Outline each Plasmodium falciparum-infected red blood cell.
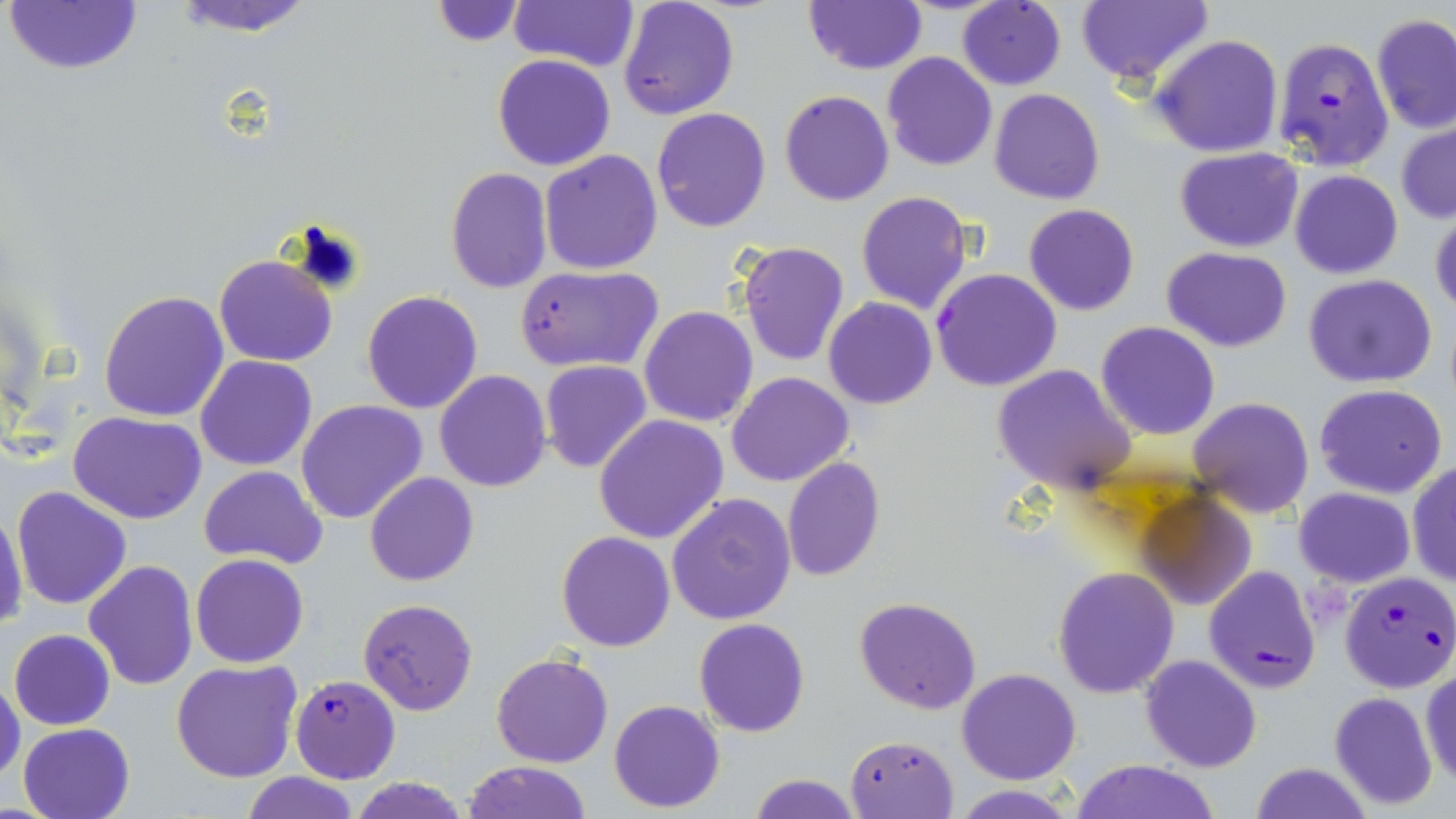

Approximate bounding boxes as [x1, y1, x2, y2] in pixels.
Plasmodium falciparum-infected red blood cells: [1272, 35, 1394, 171], [931, 268, 1061, 392], [1203, 565, 1320, 693], [1339, 572, 1456, 695], [291, 675, 399, 784].

slide_level_diagnosis: Plasmodium falciparum
modality: light microscopy
magnification: 1000x
preparation: thin blood smear
field_of_view: one of a larger specimen
image_size: 1456×819 pixels
uninfected_red_blood_cell_locations: 'approximate bounding boxes as [x1, y1, x2, y2] in pixels: [170, 0, 316, 36], [803, 0, 928, 75], [957, 0, 1066, 90], [4, 1, 142, 74], [429, 1, 526, 48], [511, 1, 638, 71], [617, 1, 740, 120], [1076, 1, 1213, 87], [1371, 13, 1456, 133], [1151, 33, 1284, 157], [882, 51, 997, 171], [492, 54, 614, 170], [990, 88, 1104, 204], [779, 91, 894, 207], [651, 107, 771, 233], [1396, 121, 1456, 224], [1175, 148, 1304, 252], [539, 150, 664, 276], [444, 167, 553, 295], [1289, 169, 1402, 278], [857, 190, 972, 314], [1025, 204, 1138, 316], [1431, 210, 1456, 318], [738, 241, 850, 367], [1162, 247, 1291, 350], [214, 254, 338, 367], [516, 265, 663, 373], [1303, 273, 1439, 387], [98, 290, 229, 422], [361, 290, 483, 414], [824, 297, 936, 409], [639, 305, 759, 427], [1096, 322, 1221, 441], [197, 356, 317, 470], [539, 361, 652, 474], [991, 365, 1135, 495], [434, 370, 553, 492], [727, 372, 855, 488], [1313, 384, 1448, 499], [1187, 397, 1313, 519], [295, 399, 428, 523], [68, 411, 207, 525], [595, 414, 729, 543], [783, 456, 884, 582], [1408, 460, 1456, 587], [199, 465, 328, 567], [364, 472, 479, 587], [11, 485, 132, 610], [1293, 486, 1415, 588], [1139, 491, 1257, 609], [666, 493, 798, 626], [0, 507, 27, 636], [555, 531, 675, 652], [190, 554, 310, 668], [83, 559, 198, 688], [1053, 566, 1180, 699], [855, 596, 981, 714], [357, 598, 479, 716], [694, 618, 811, 737], [8, 629, 114, 730], [492, 652, 614, 769], [1140, 655, 1261, 772], [171, 659, 303, 783], [956, 668, 1081, 785], [1419, 668, 1456, 789], [0, 677, 24, 786], [1329, 691, 1438, 810], [608, 698, 726, 813], [19, 722, 135, 819], [845, 734, 958, 818], [1069, 759, 1222, 819], [462, 761, 592, 819], [1250, 763, 1371, 819], [242, 772, 359, 819], [749, 774, 864, 818], [348, 776, 472, 819], [952, 784, 1079, 819]'
stain: May-Grünwald-Giemsa